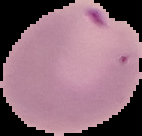
Result: malaria parasites detected. The area outside the segmented cell region is set to black. Image is 142×136 pixels. From a thin blood smear.